Assess this cell for malaria.
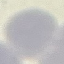
Uninfected.

image type = cell patch, automatically extracted from a larger field of view and resized to 64 × 64 pixels
stain = Giemsa
preparation = thin blood smear
capture = smartphone through the microscope eyepiece